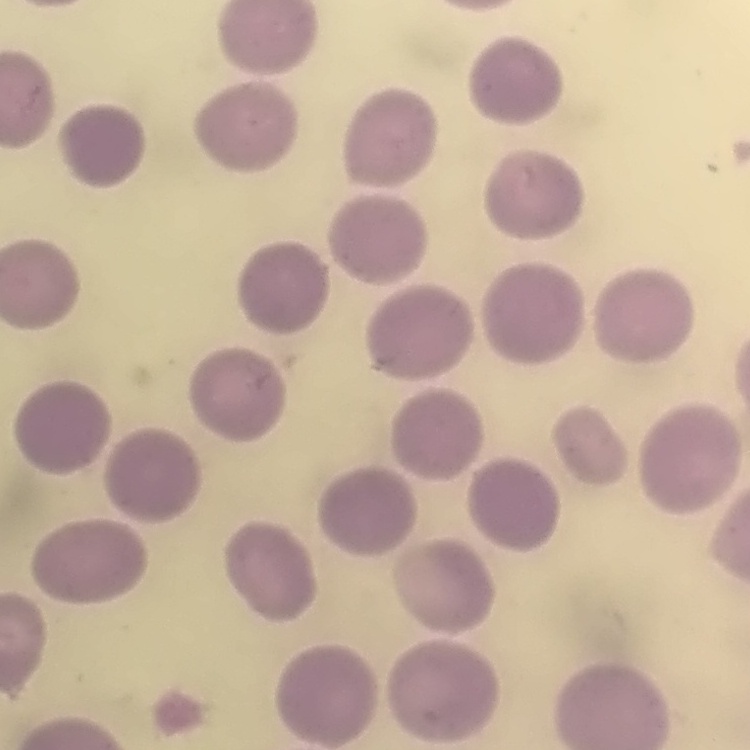
The red blood cells show no rouleaux formation. Thin blood smear. Square crop of a larger photomicrograph. Field's or Giemsa stain.